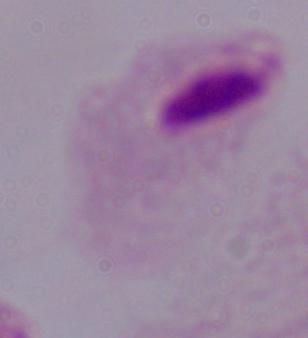

Summary:
  - Magnification: 1000x
  - Identification: trichomonad
  - Modality: micrograph